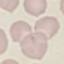

{
  "malaria_status": "uninfected",
  "capture": "smartphone through the microscope eyepiece",
  "stain": "Giemsa",
  "image_type": "cell patch, automatically extracted from a larger field of view and resized to 64 × 64 pixels",
  "preparation": "thin smear"
}